Comment on the morphology of the erythrocytes.
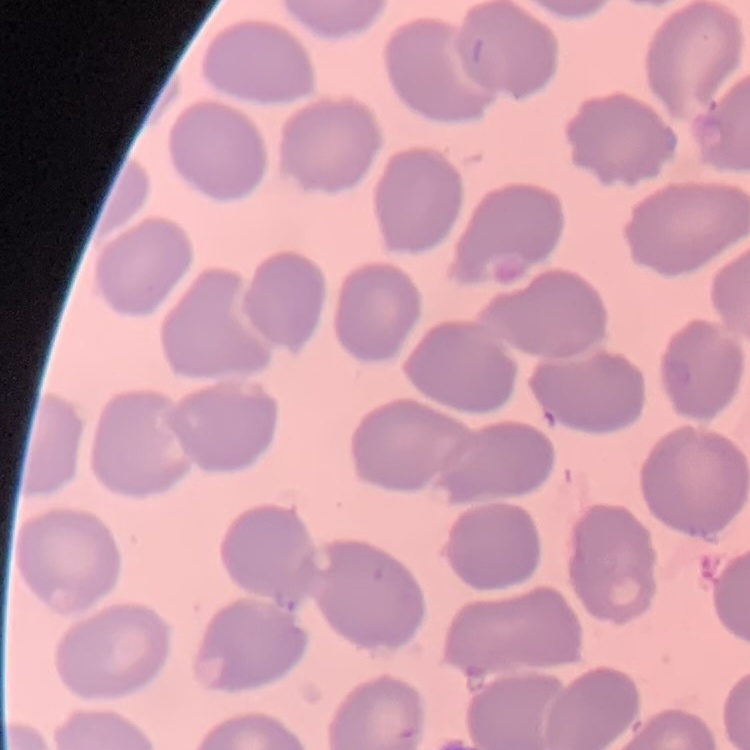
No rouleaux formation.

preparation: thin blood film
image_type: square crop of a larger photomicrograph
stain: Field's or Giemsa